Describe the morphology of the red blood cells.
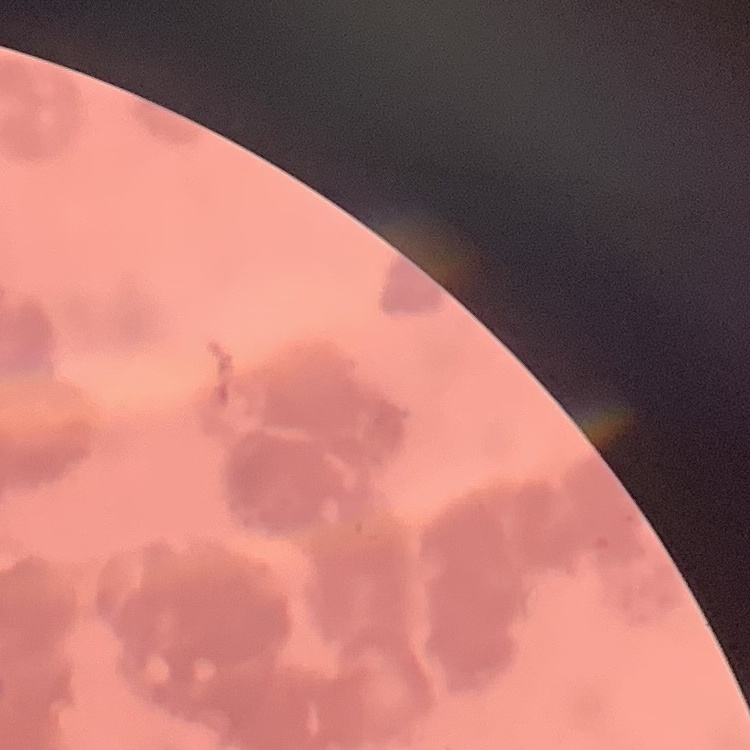

Rouleaux formation.

One tile cut from a larger photomicrograph. Thin blood smear. Field's or Giemsa stain.